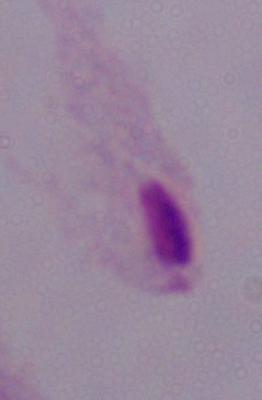

Summary:
  - Magnification: 1000x
  - Identification: trichomonad
  - Modality: micrograph